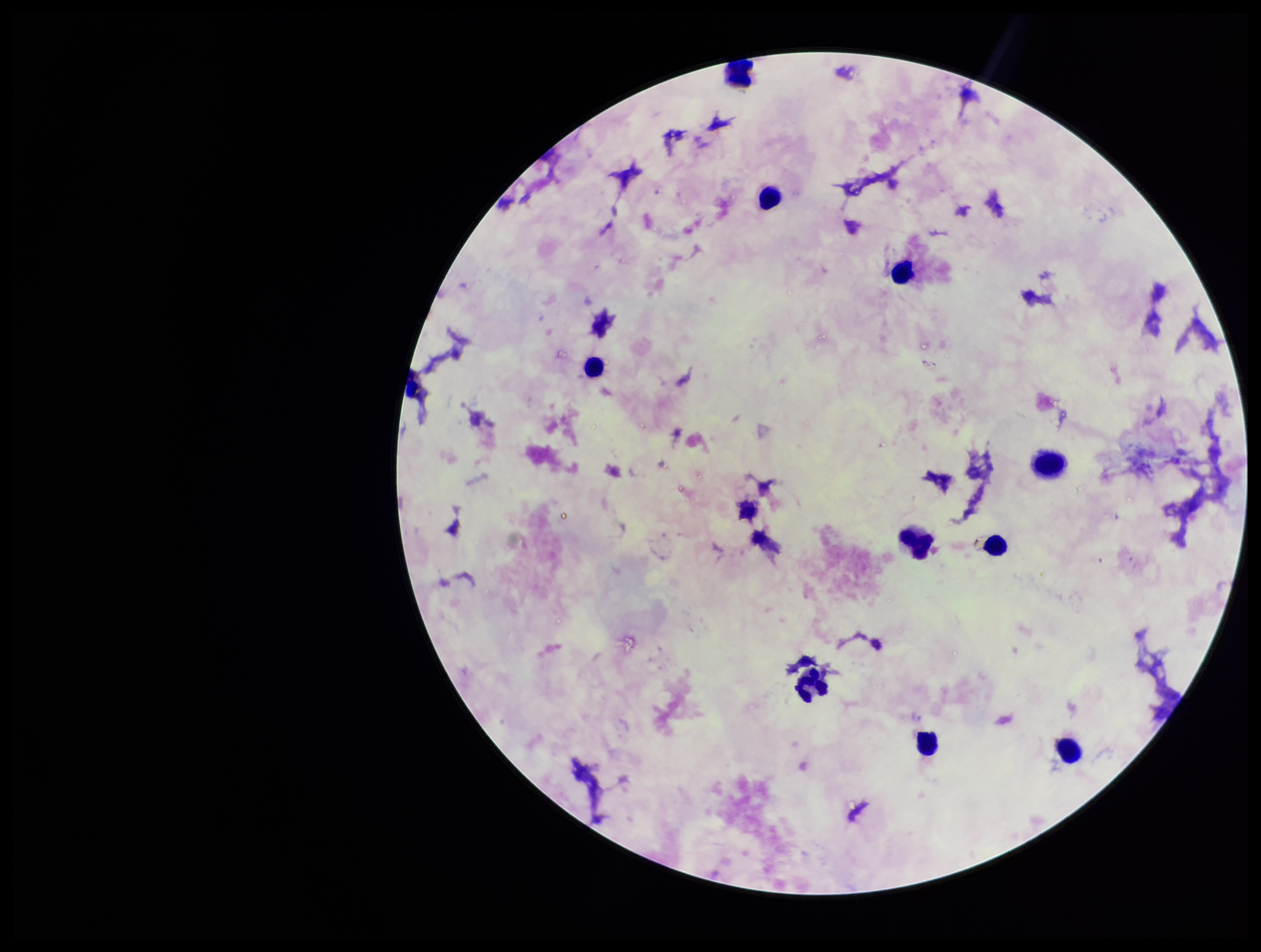
Summary:
  - Patient malaria status: negative
  - Field of view: one from this slide
  - Image size: 1261×952 pixels
  - Plasmodium parasites: none detected
  - Capture: smartphone photograph through the microscope eyepiece
  - Stain: Giemsa
  - Preparation: thick
  - Parasite count: 0
  - Leukocyte count: 10